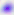
Photomicrograph. Toxoplasma gondii is shown. 400x magnification.